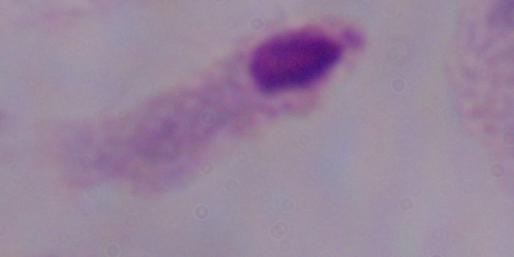

identification = trichomonad
magnification = 1000x
modality = photomicrograph